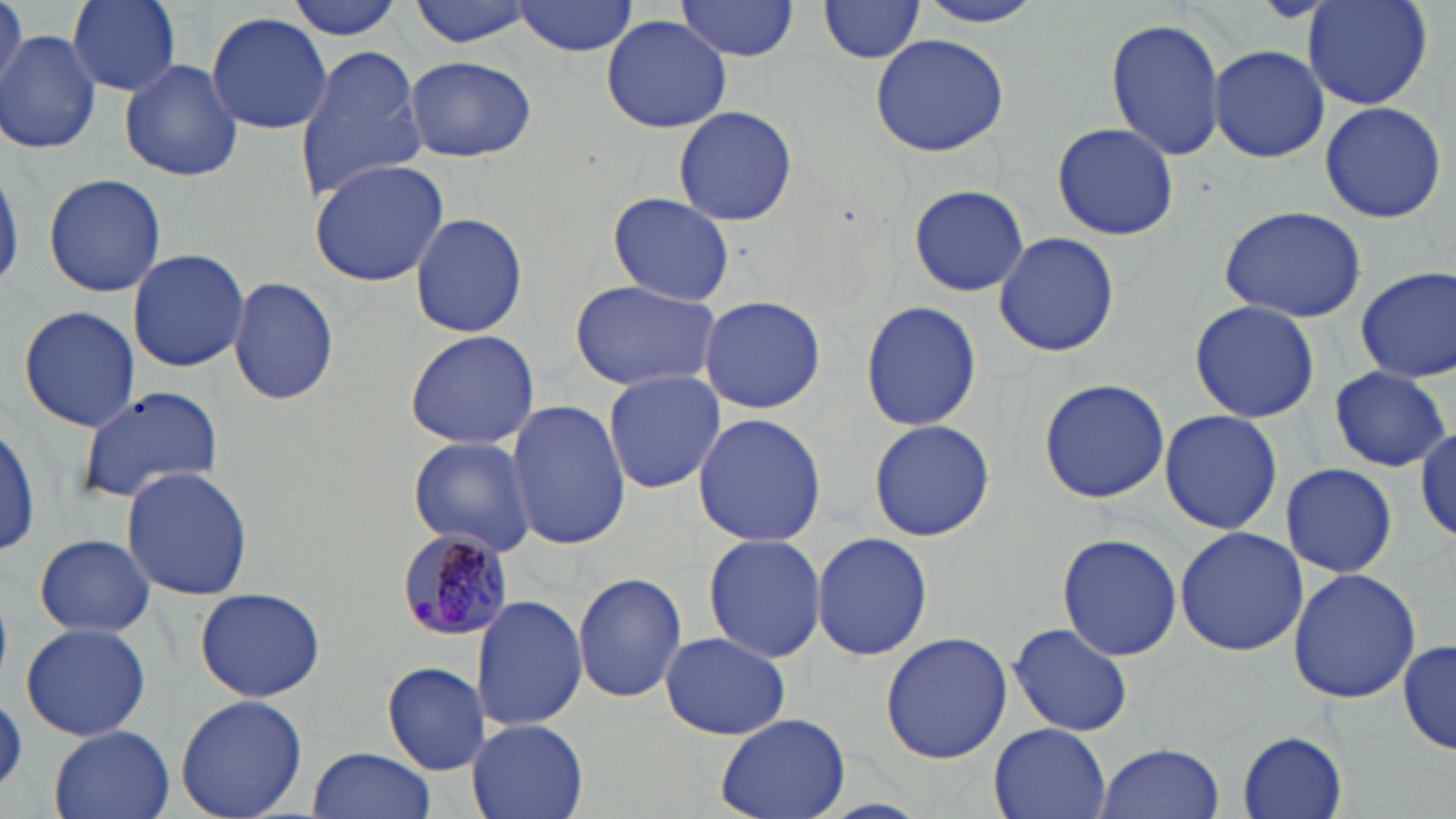
Approximate bounding boxes as (x1, y1, x2, y2) in pixels. Plasmodium malariae-infected red blood cell locations: (394, 528, 516, 642). Uninfected red blood cell locations: (0, 0, 24, 94), (68, 0, 183, 94), (283, 0, 409, 40), (407, 0, 544, 50), (515, 0, 639, 57), (910, 0, 1052, 27), (1303, 0, 1433, 111), (673, 2, 802, 65), (817, 2, 925, 64), (206, 11, 334, 136), (600, 13, 733, 133), (1104, 15, 1226, 163), (2, 29, 101, 154), (868, 31, 1010, 158), (292, 42, 430, 203), (1208, 44, 1328, 163), (404, 55, 535, 162), (119, 58, 244, 181), (1318, 100, 1448, 224), (670, 104, 800, 227), (1052, 123, 1178, 239), (307, 159, 449, 286), (0, 161, 22, 294), (42, 173, 166, 298), (908, 183, 1030, 297), (606, 191, 735, 307), (1218, 206, 1367, 322), (409, 211, 530, 338), (992, 232, 1120, 358), (127, 247, 251, 373), (1354, 267, 1456, 383), (228, 276, 339, 408), (570, 280, 722, 393), (699, 294, 826, 414), (1189, 300, 1320, 425), (860, 301, 982, 432), (16, 305, 142, 432), (405, 327, 540, 451), (1327, 366, 1450, 473), (603, 372, 727, 494), (1038, 378, 1170, 503), (77, 385, 225, 504), (505, 398, 630, 552), (1159, 408, 1282, 534), (692, 413, 827, 547), (868, 420, 994, 541), (0, 422, 41, 561), (1415, 427, 1456, 545), (408, 435, 538, 558), (1280, 463, 1397, 577), (120, 465, 255, 600), (1174, 528, 1309, 657), (811, 532, 933, 662), (1057, 532, 1181, 661), (33, 534, 157, 639), (703, 535, 827, 664), (1288, 568, 1422, 704), (574, 571, 689, 704), (193, 587, 326, 702), (472, 596, 587, 731), (1008, 622, 1133, 737), (19, 623, 151, 742), (660, 632, 791, 741), (879, 632, 1012, 765), (1398, 640, 1455, 757), (382, 662, 490, 774), (175, 694, 308, 818), (717, 713, 851, 819), (467, 718, 589, 819), (990, 723, 1110, 819), (48, 727, 175, 819), (1238, 731, 1349, 817), (1095, 741, 1226, 819), (307, 745, 435, 818). Slide-level diagnosis: Plasmodium malariae. 1000x magnification. May-Grünwald-Giemsa stain. Image is 1456×819 pixels. Light microscopy. Single field of view. Thin blood smear.